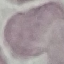
Summary:
  - Result: no malaria parasites seen
  - Preparation: thin blood smear
  - Capture: smartphone camera at the microscope eyepiece
  - Image type: cell patch, automatically extracted from a larger field of view and resized to 64 × 64 pixels
  - Stain: Giemsa